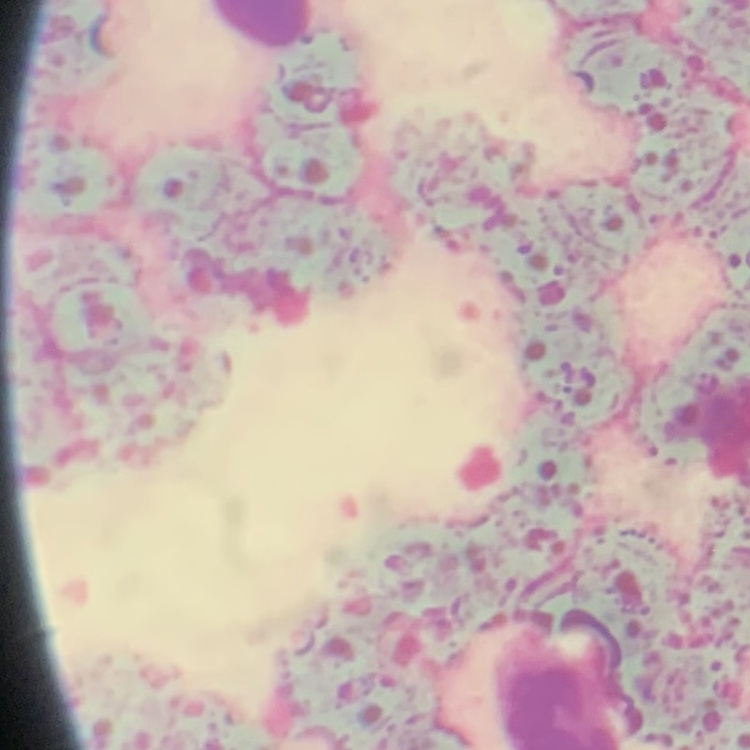
The red blood cells show rouleaux formation. Thin blood film. One tile cut from a larger photomicrograph. Field's or Giemsa stain.